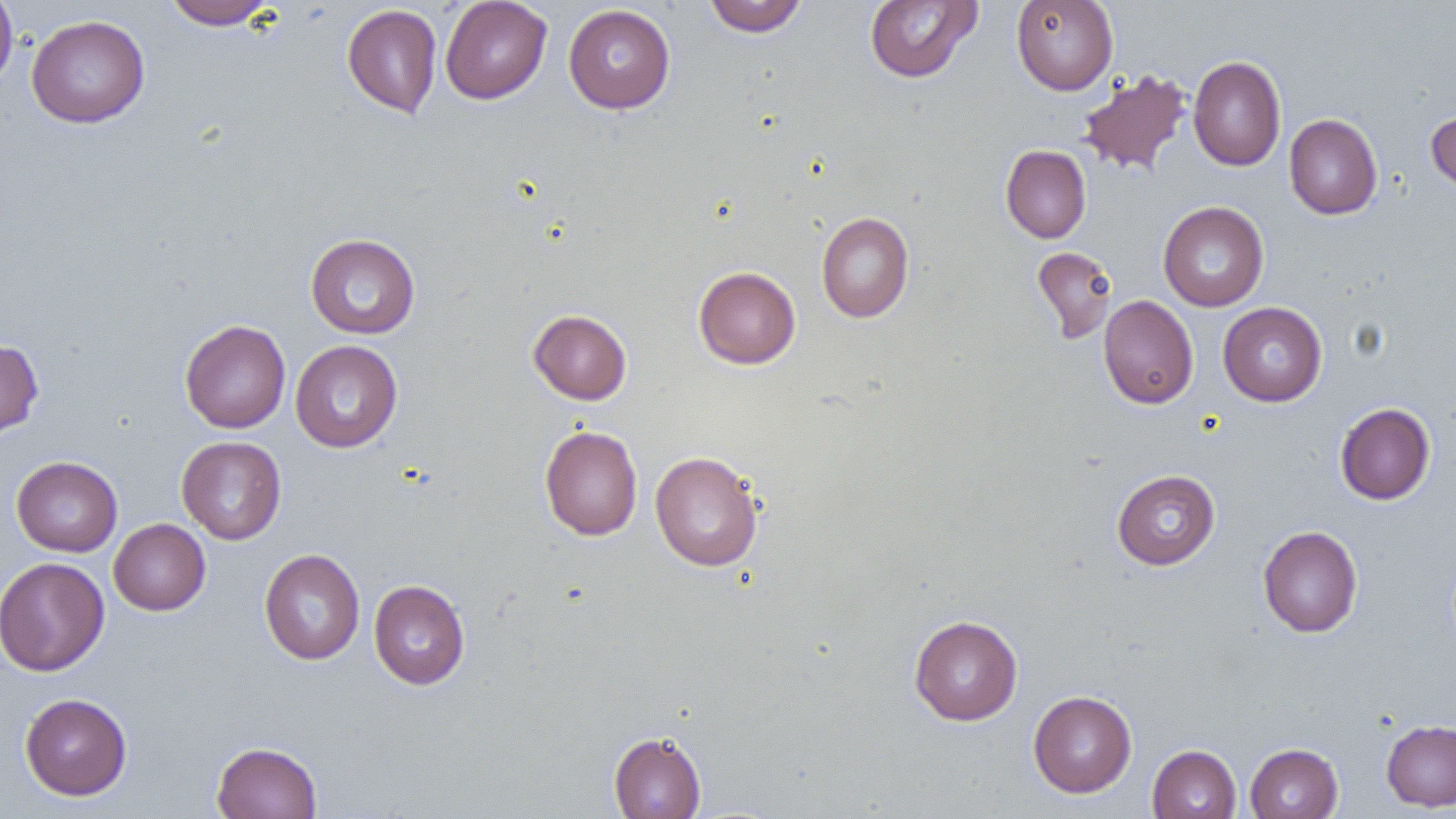
Approximate bounding boxes as (x1,y1)-(x2,y2) corner pairs in pixels. Uninfected red blood cell locations: (0,0)-(19,91), (162,0)-(277,30), (439,0)-(552,104), (703,0)-(808,37), (1011,0)-(1118,95), (864,1)-(982,83), (341,4)-(442,119), (563,4)-(675,113), (26,14)-(150,128), (1188,55)-(1286,171), (1077,68)-(1193,178), (1426,109)-(1456,197), (1284,114)-(1382,219), (1000,145)-(1091,243), (1158,202)-(1268,311), (816,211)-(914,323), (305,233)-(421,339), (1031,246)-(1118,345), (693,266)-(801,369), (1098,295)-(1198,409), (1218,302)-(1327,406), (528,309)-(632,405), (179,319)-(291,433), (0,339)-(44,440), (290,340)-(403,453), (1334,402)-(1435,505), (539,425)-(643,541), (176,436)-(287,544), (650,451)-(764,572), (11,456)-(122,557), (1112,469)-(1221,570), (109,519)-(210,615), (1258,525)-(1363,637), (259,548)-(365,665), (0,557)-(110,676), (368,579)-(470,689), (909,614)-(1022,725), (1028,690)-(1137,798), (20,693)-(132,800), (1382,719)-(1456,811), (608,730)-(706,818), (211,741)-(322,819), (1245,743)-(1343,818), (1147,744)-(1241,819). Slide-level diagnosis: no evidence of blood parasites. One field of a larger specimen. Thin blood film. 1000x magnification. Optical microscopy. Image is 1456×819 pixels.